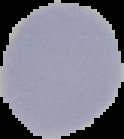
Summary:
  - Preparation: thin blood film
  - Result: negative for Plasmodium parasites
  - Image type: cell region segmented out of the field of view; surrounding area masked to black
  - Image size: 124×139 pixels